Identify the parasite.
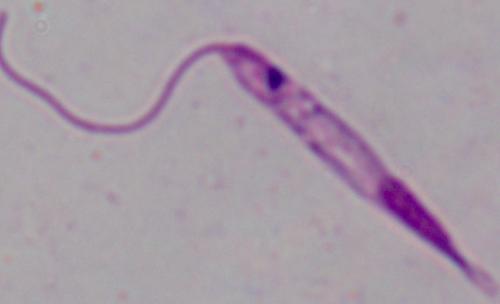

This is Leishmania.

1000x magnification. Photomicrograph.